Give the position of every malaria parasite.
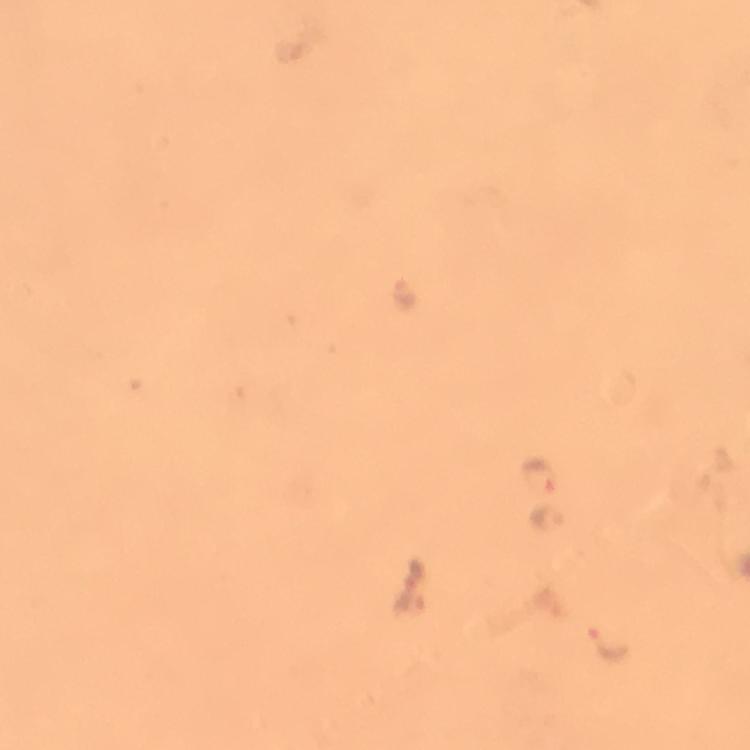

Approximate centers as {x, y} in pixels.
Malaria parasites: {545, 474}, {548, 519}, {611, 644}.

Summary:
  - Cropped from: a single field of view
  - Magnification: 100x
  - Stain: Giemsa
  - Image size: 750×750 pixels
  - Context: from a malaria diagnostic workup
  - Capture: smartphone mounted on the microscope
  - Immersion oil: used
  - Preparation: thick smear